Classify this cell by malaria status.
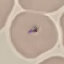

Uninfected.

Automatically extracted cell patch, resized to 64 × 64 pixels. Acquired by smartphone through the microscope eyepiece. Thin blood smear. Giemsa-stained preparation.